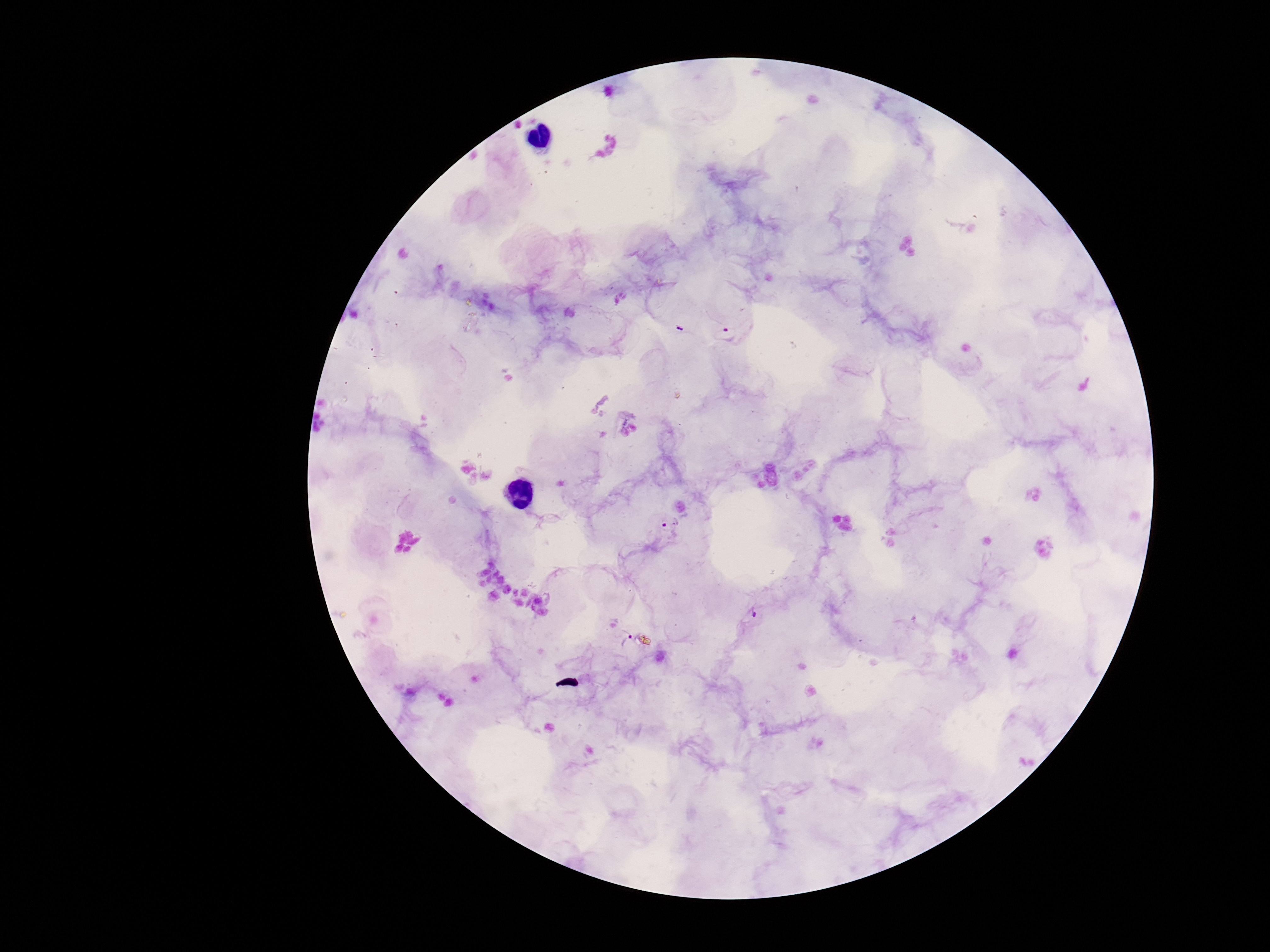
{
  "capture": "smartphone camera through the microscope eyepiece",
  "plasmodium_parasite_locations": "approximate centers as {x, y} in pixels: {726, 334}, {669, 520}, {753, 610}, {621, 638}",
  "field_of_view": "one from this slide",
  "magnification": "100x",
  "stain": "Giemsa",
  "preparation": "thick peripheral-blood smear",
  "patient_malaria_status": "positive",
  "image_size": "1270×952 pixels"
}